Point out each leukocyte.
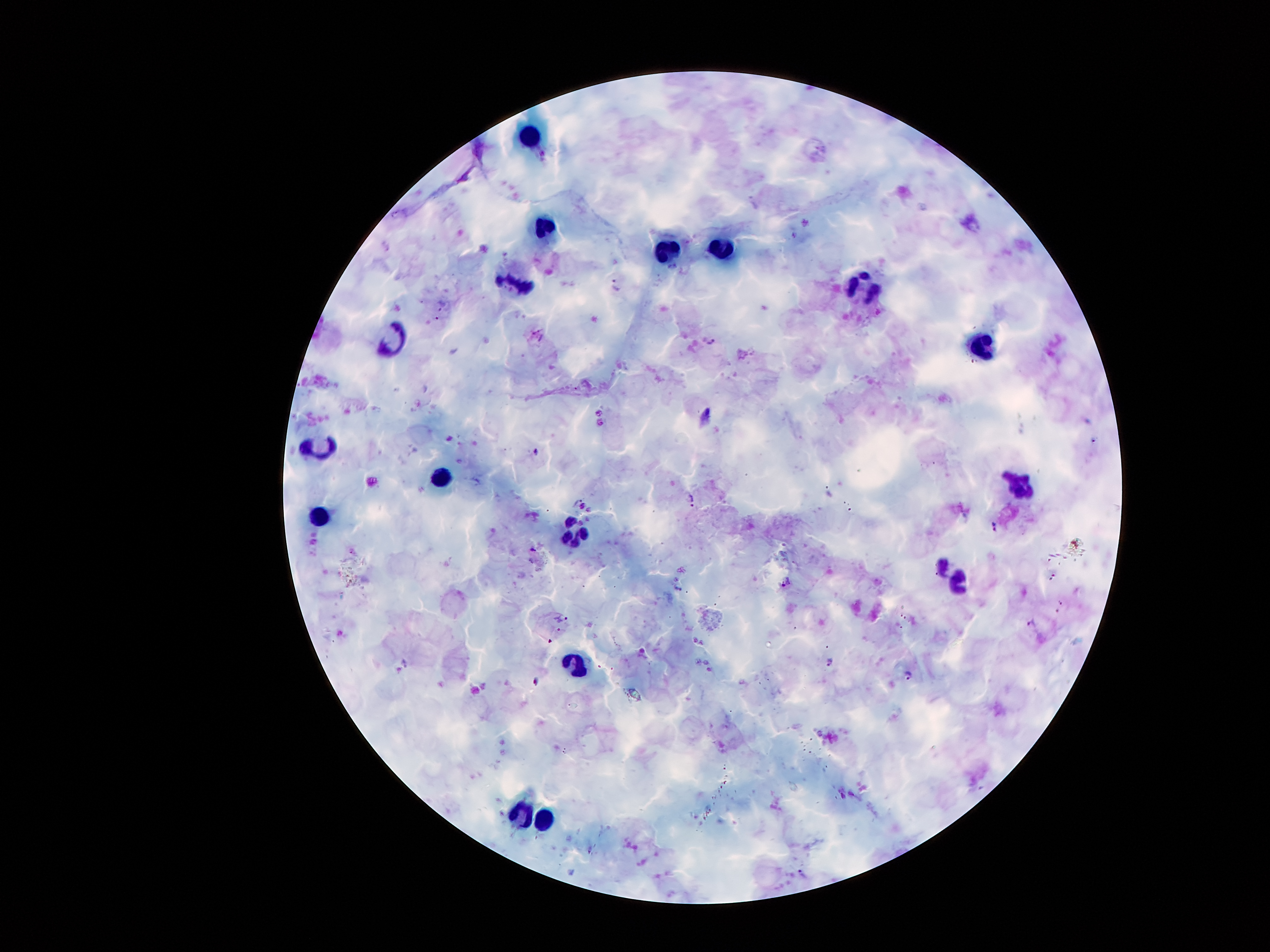
Approximate object centers, in pixels from the top-left corner.
Leukocytes: (x=531, y=137), (x=546, y=226), (x=664, y=247), (x=724, y=249), (x=520, y=284), (x=861, y=289), (x=396, y=339), (x=981, y=344), (x=320, y=452), (x=438, y=475), (x=1021, y=483), (x=320, y=518), (x=572, y=533), (x=960, y=581), (x=578, y=665), (x=519, y=812), (x=544, y=820).

malaria parasite locations = (x=617, y=285), (x=711, y=341), (x=538, y=452), (x=692, y=500), (x=994, y=527), (x=533, y=550), (x=786, y=582), (x=678, y=589), (x=830, y=661), (x=908, y=676), (x=535, y=681), (x=802, y=872)
image size = 1270×952 pixels
preparation = thick peripheral-blood smear
capture = smartphone through the microscope eyepiece
patient malaria status = positive for Plasmodium falciparum
field of view = one from this slide
stain = Giemsa
magnification = 100x